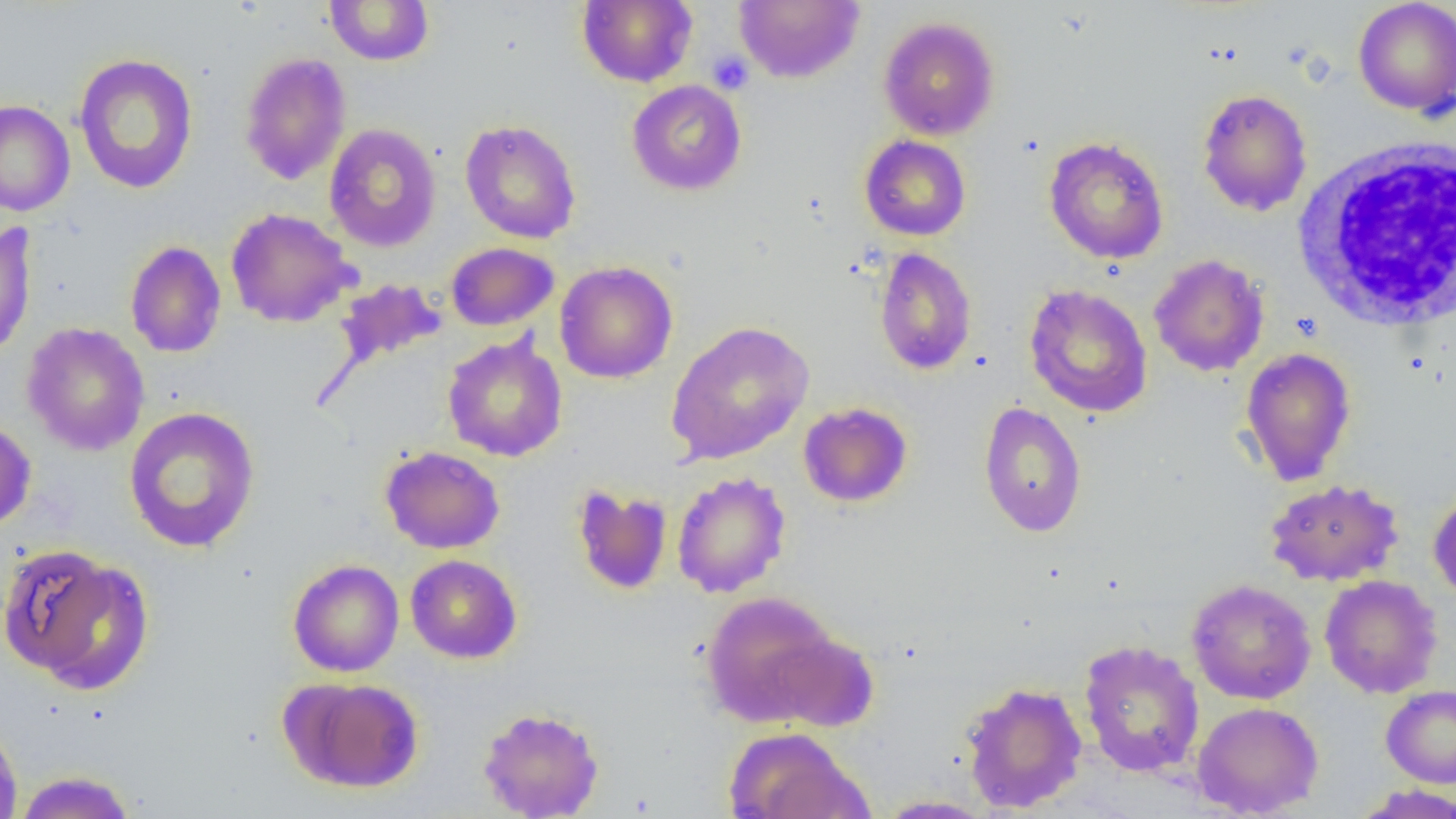
slide-level diagnosis = negative for blood parasites
preparation = thin blood film
image size = 1456×819 pixels
modality = light microscopy
magnification = 1000x
field of view = one of a larger specimen
platelet locations = approximate bounding boxes as (x1,y1)-(x2,y2) corner pairs in pixels: (707,50)-(753,95)
white blood cell locations = approximate bounding boxes as (x1,y1)-(x2,y2) corner pairs in pixels: (1291,137)-(1455,332)
uninfected red blood cell locations = approximate bounding boxes as (x1,y1)-(x2,y2) corner pairs in pixels: (324,0)-(435,66), (577,0)-(697,87), (733,0)-(865,84), (1353,0)-(1456,117), (878,16)-(1000,141), (239,52)-(351,186), (73,53)-(199,194), (627,80)-(747,196), (1196,88)-(1313,216), (0,100)-(75,216), (460,119)-(581,244), (324,123)-(441,252), (859,135)-(971,241), (1044,136)-(1169,264), (225,208)-(357,327), (0,222)-(37,362), (125,241)-(226,358), (446,242)-(559,331), (874,247)-(977,376), (1149,254)-(1269,377), (554,261)-(678,384), (334,278)-(447,369), (1024,284)-(1154,418), (665,321)-(814,465), (21,322)-(150,456), (442,334)-(568,462), (1240,347)-(1357,486), (978,401)-(1087,538), (798,402)-(913,508), (124,406)-(261,553), (0,419)-(36,531), (379,446)-(505,554), (671,471)-(791,598), (1265,478)-(1404,586), (571,484)-(674,595), (1428,490)-(1456,601), (1,544)-(151,693), (406,554)-(522,664), (287,558)-(404,677), (1319,574)-(1443,698), (1186,579)-(1316,705), (701,590)-(844,727), (1078,639)-(1205,777), (283,676)-(425,793), (960,681)-(1088,813), (1381,684)-(1456,788), (1192,701)-(1324,817), (477,706)-(605,818), (0,718)-(23,819), (722,726)-(870,819), (13,770)-(138,818), (1351,784)-(1456,819), (874,795)-(996,818)